Locate every malaria parasite and every leukocyte.
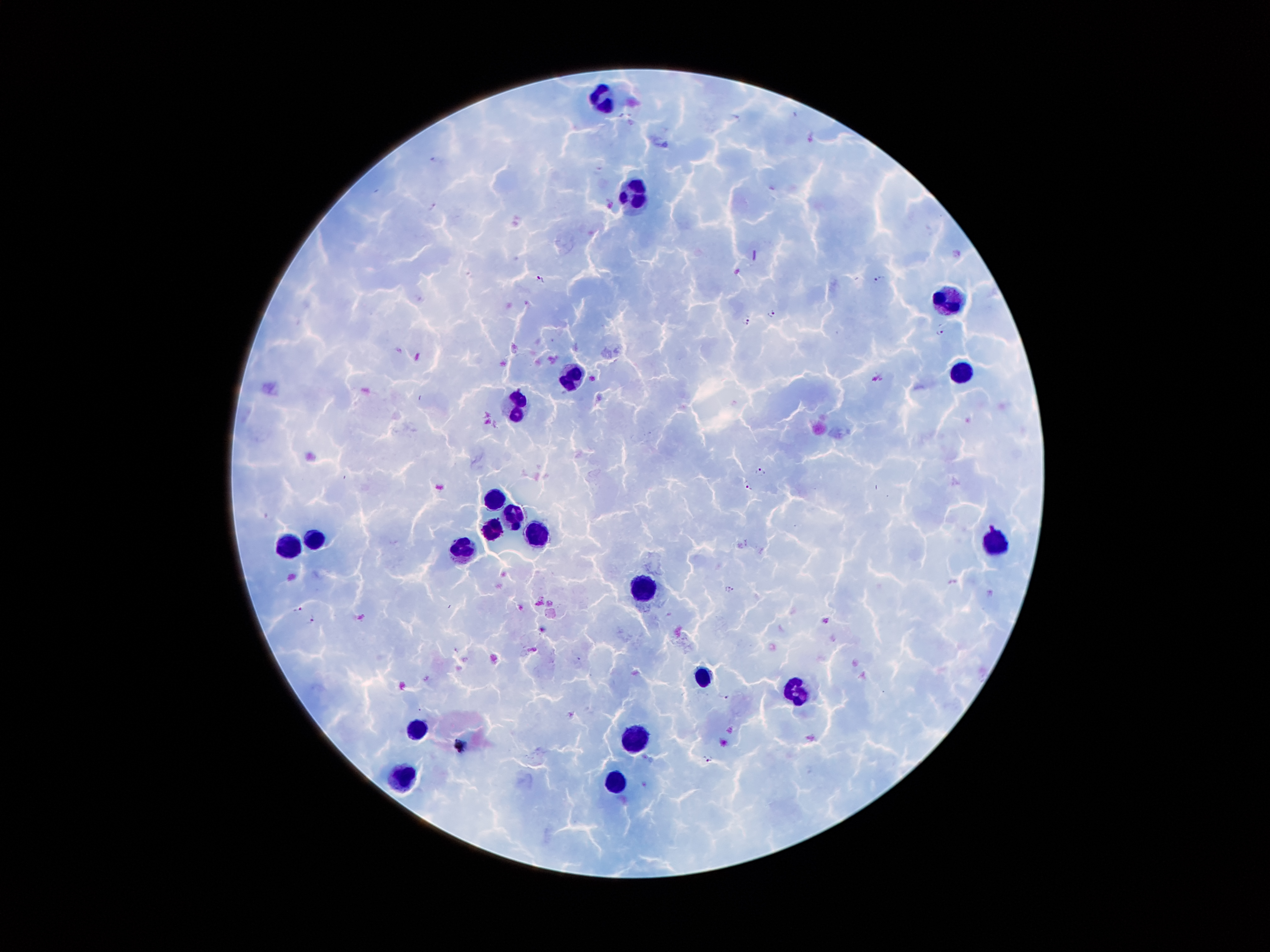
Approximate centers as (x, y) in pixels.
Malaria parasites: (736, 116), (433, 158), (432, 205), (611, 206), (539, 279), (877, 279), (772, 314), (746, 320), (940, 333), (760, 471), (747, 484), (728, 589), (298, 609), (312, 620), (456, 650), (725, 697), (420, 710), (459, 745), (708, 758).
Leukocytes: (602, 98), (636, 192), (950, 300), (962, 370), (573, 377), (518, 405), (495, 498), (517, 515), (492, 530), (537, 531), (316, 539), (997, 544), (291, 549), (464, 551), (639, 586), (702, 675), (794, 692), (416, 726), (636, 740), (401, 776), (614, 782).

Giemsa stain. Single field of view. Patient malaria status: positive for Plasmodium falciparum. Image is 1270×952 pixels. Smartphone photograph taken through the microscope eyepiece. 100x magnification. Thick blood smear.